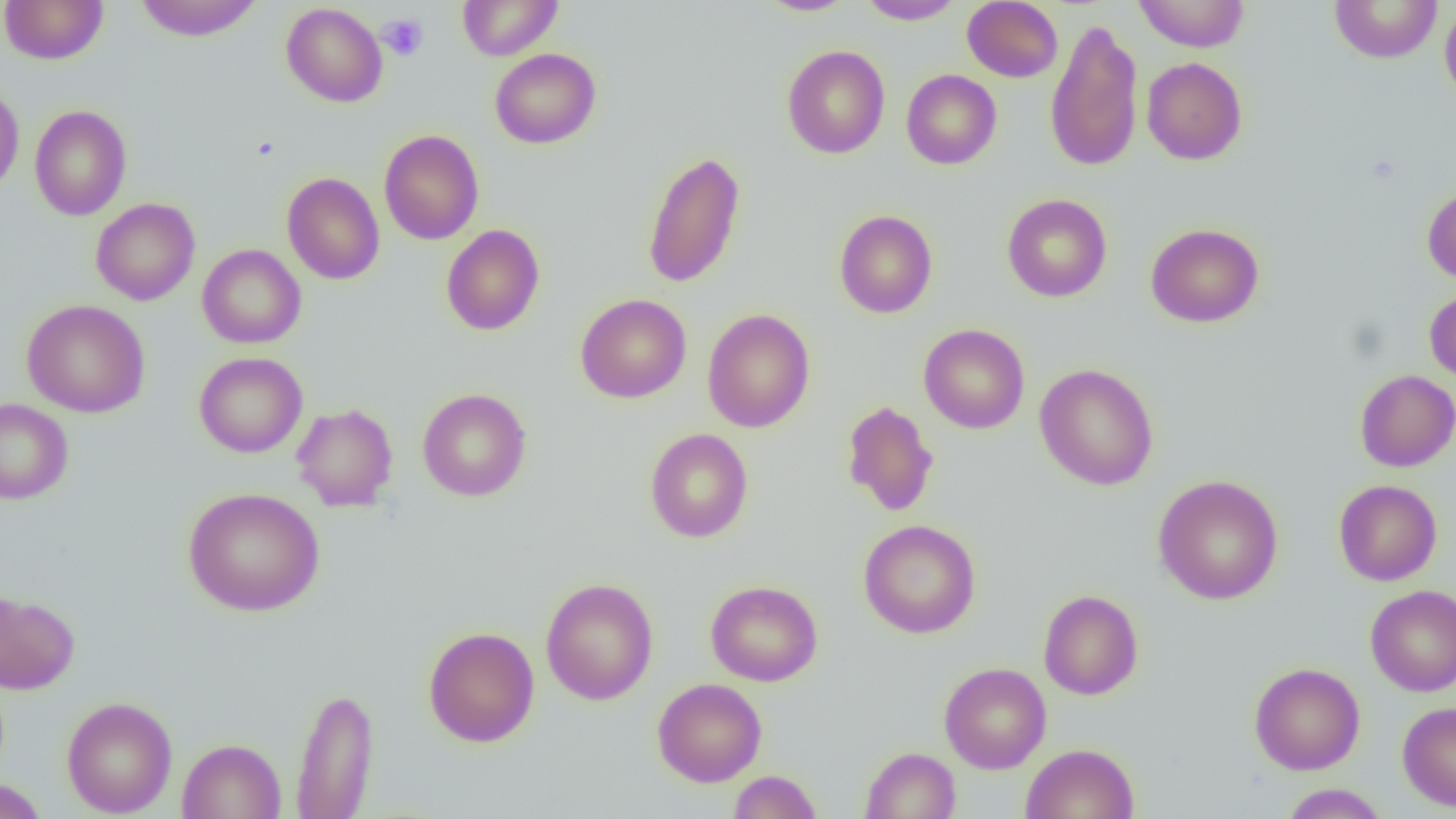
Summary:
  - Coordinate format: approximate bounding boxes as (x1,y1)-(x2,y2) corner pairs in pixels
  - Platelet locations: (378,13)-(428,61)
  - Uninfected red blood cell locations: (0,0)-(108,65), (133,0)-(265,41), (457,0)-(562,60), (757,0)-(859,17), (857,0)-(964,25), (1133,0)-(1250,52), (962,1)-(1063,82), (1329,1)-(1443,63), (281,3)-(388,107), (1440,4)-(1456,106), (1044,16)-(1145,173), (781,45)-(890,159), (489,48)-(601,149), (1142,57)-(1247,165), (901,69)-(1002,169), (0,81)-(24,196), (29,105)-(132,221), (379,129)-(484,245), (642,149)-(746,289), (282,172)-(385,285), (1422,186)-(1456,283), (1001,194)-(1112,302), (90,198)-(200,306), (834,210)-(938,318), (1145,223)-(1264,327), (441,225)-(545,335), (197,244)-(306,348), (1424,288)-(1456,385), (575,293)-(691,403), (22,299)-(150,417), (702,308)-(816,432), (918,323)-(1030,434), (194,352)-(308,458), (1034,363)-(1159,491), (1355,369)-(1456,472), (417,388)-(531,502), (0,398)-(73,504), (841,400)-(939,517), (292,403)-(399,512), (644,428)-(753,543), (1153,474)-(1284,605), (1334,479)-(1442,585), (182,487)-(325,615), (858,519)-(981,638), (541,577)-(658,705), (705,580)-(822,686), (1365,584)-(1456,697), (0,589)-(80,694), (1038,589)-(1144,700), (423,626)-(539,747), (939,662)-(1051,773), (1249,662)-(1365,775), (652,677)-(767,787), (290,686)-(379,818), (61,696)-(177,817), (1397,701)-(1456,811), (177,738)-(286,819), (1021,743)-(1140,819), (860,747)-(961,818), (728,770)-(822,819), (0,779)-(49,819), (1281,783)-(1389,818)
  - Slide-level diagnosis: no evidence of blood parasites
  - Preparation: thin blood smear
  - Image size: 1456×819 pixels
  - Modality: light microscopy
  - Field of view: single
  - Magnification: 1000x